Report the malaria status of this cell.
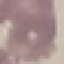
Uninfected.

Cell patch, automatically extracted from a larger field of view and resized to 64 × 64 pixels. Thin smear of blood. Acquired by smartphone through the microscope eyepiece. Giemsa-stained preparation.